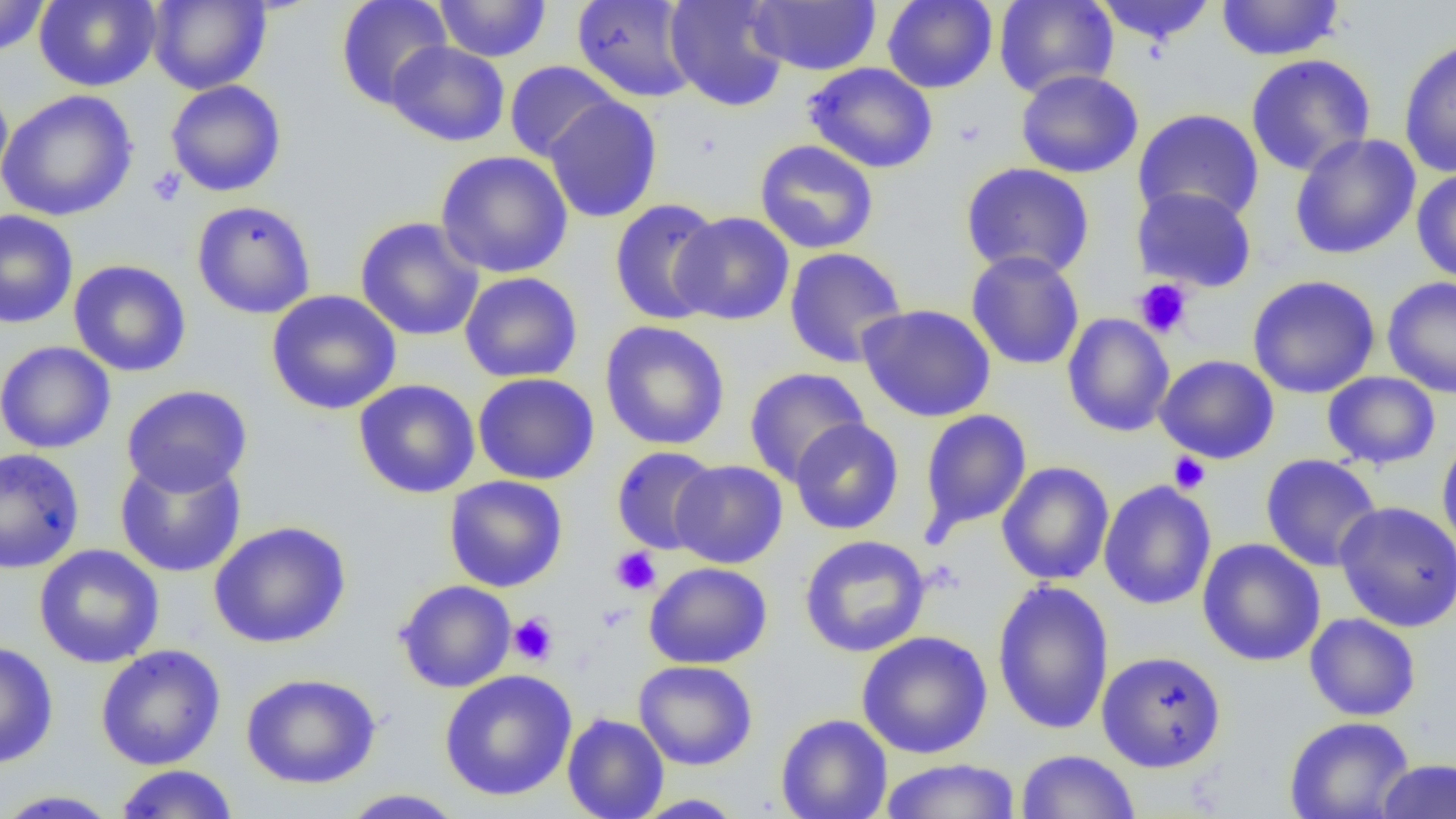 Approximate bounding boxes as named x1/y1/x2/y2 corners in pixels. Uninfected red blood cell locations: (x1=0, y1=0, x2=51, y2=57), (x1=34, y1=0, x2=161, y2=91), (x1=335, y1=0, x2=452, y2=110), (x1=434, y1=0, x2=551, y2=62), (x1=571, y1=0, x2=698, y2=103), (x1=665, y1=0, x2=790, y2=112), (x1=881, y1=0, x2=998, y2=93), (x1=994, y1=0, x2=1119, y2=99), (x1=1094, y1=0, x2=1217, y2=45), (x1=1215, y1=0, x2=1345, y2=61), (x1=148, y1=1, x2=271, y2=94), (x1=747, y1=1, x2=881, y2=75), (x1=1398, y1=37, x2=1456, y2=179), (x1=386, y1=40, x2=510, y2=147), (x1=1245, y1=54, x2=1376, y2=176), (x1=504, y1=60, x2=621, y2=163), (x1=804, y1=62, x2=938, y2=174), (x1=1015, y1=69, x2=1143, y2=178), (x1=165, y1=79, x2=287, y2=197), (x1=0, y1=82, x2=13, y2=197), (x1=0, y1=89, x2=138, y2=222), (x1=543, y1=95, x2=663, y2=223), (x1=1132, y1=107, x2=1264, y2=226), (x1=1289, y1=133, x2=1421, y2=260), (x1=754, y1=139, x2=879, y2=254), (x1=435, y1=150, x2=574, y2=278), (x1=960, y1=162, x2=1095, y2=280), (x1=1411, y1=168, x2=1456, y2=284), (x1=1131, y1=185, x2=1258, y2=293), (x1=609, y1=197, x2=725, y2=326), (x1=191, y1=200, x2=317, y2=319), (x1=0, y1=210, x2=78, y2=329), (x1=670, y1=211, x2=795, y2=325), (x1=354, y1=216, x2=485, y2=342), (x1=784, y1=247, x2=908, y2=369), (x1=966, y1=250, x2=1085, y2=371), (x1=68, y1=260, x2=191, y2=377), (x1=459, y1=271, x2=583, y2=383), (x1=1247, y1=274, x2=1381, y2=399), (x1=1382, y1=276, x2=1456, y2=398), (x1=266, y1=290, x2=402, y2=415), (x1=856, y1=303, x2=996, y2=423), (x1=1062, y1=312, x2=1175, y2=436), (x1=599, y1=320, x2=731, y2=450), (x1=0, y1=341, x2=116, y2=454), (x1=1155, y1=354, x2=1279, y2=464), (x1=744, y1=367, x2=870, y2=487), (x1=1322, y1=371, x2=1441, y2=470), (x1=472, y1=372, x2=600, y2=485), (x1=353, y1=379, x2=481, y2=498), (x1=121, y1=384, x2=253, y2=497), (x1=918, y1=409, x2=1032, y2=539), (x1=789, y1=417, x2=904, y2=535), (x1=1436, y1=435, x2=1456, y2=556), (x1=611, y1=446, x2=721, y2=555), (x1=0, y1=447, x2=85, y2=575), (x1=114, y1=453, x2=247, y2=578), (x1=1260, y1=454, x2=1383, y2=572), (x1=669, y1=459, x2=788, y2=569), (x1=996, y1=461, x2=1114, y2=585), (x1=444, y1=475, x2=568, y2=593), (x1=1098, y1=480, x2=1216, y2=610), (x1=1334, y1=500, x2=1456, y2=633), (x1=209, y1=521, x2=351, y2=649), (x1=799, y1=534, x2=931, y2=657), (x1=1197, y1=538, x2=1325, y2=666), (x1=33, y1=544, x2=165, y2=669), (x1=644, y1=562, x2=772, y2=669), (x1=395, y1=579, x2=517, y2=693), (x1=992, y1=580, x2=1114, y2=734), (x1=1304, y1=613, x2=1421, y2=721), (x1=856, y1=630, x2=993, y2=759), (x1=0, y1=640, x2=59, y2=769), (x1=95, y1=645, x2=226, y2=770), (x1=1096, y1=650, x2=1227, y2=772), (x1=633, y1=659, x2=758, y2=770), (x1=438, y1=669, x2=577, y2=801), (x1=240, y1=672, x2=381, y2=790), (x1=562, y1=713, x2=669, y2=819), (x1=775, y1=713, x2=892, y2=819), (x1=1283, y1=716, x2=1415, y2=819), (x1=1015, y1=749, x2=1140, y2=819), (x1=879, y1=758, x2=1022, y2=818), (x1=1375, y1=758, x2=1456, y2=819), (x1=113, y1=764, x2=240, y2=818), (x1=0, y1=789, x2=122, y2=818), (x1=338, y1=789, x2=467, y2=818), (x1=631, y1=793, x2=747, y2=818). Platelet locations: (x1=147, y1=167, x2=186, y2=208), (x1=1133, y1=279, x2=1193, y2=339), (x1=1169, y1=452, x2=1211, y2=495), (x1=610, y1=547, x2=662, y2=595), (x1=596, y1=602, x2=633, y2=632), (x1=508, y1=613, x2=559, y2=666). Slide-level diagnosis: no evidence of blood parasites. One field of a larger specimen. Image is 1456×819 pixels. Light microscopy. Thin blood smear. 1000x magnification.